Identify the blood parasite species.
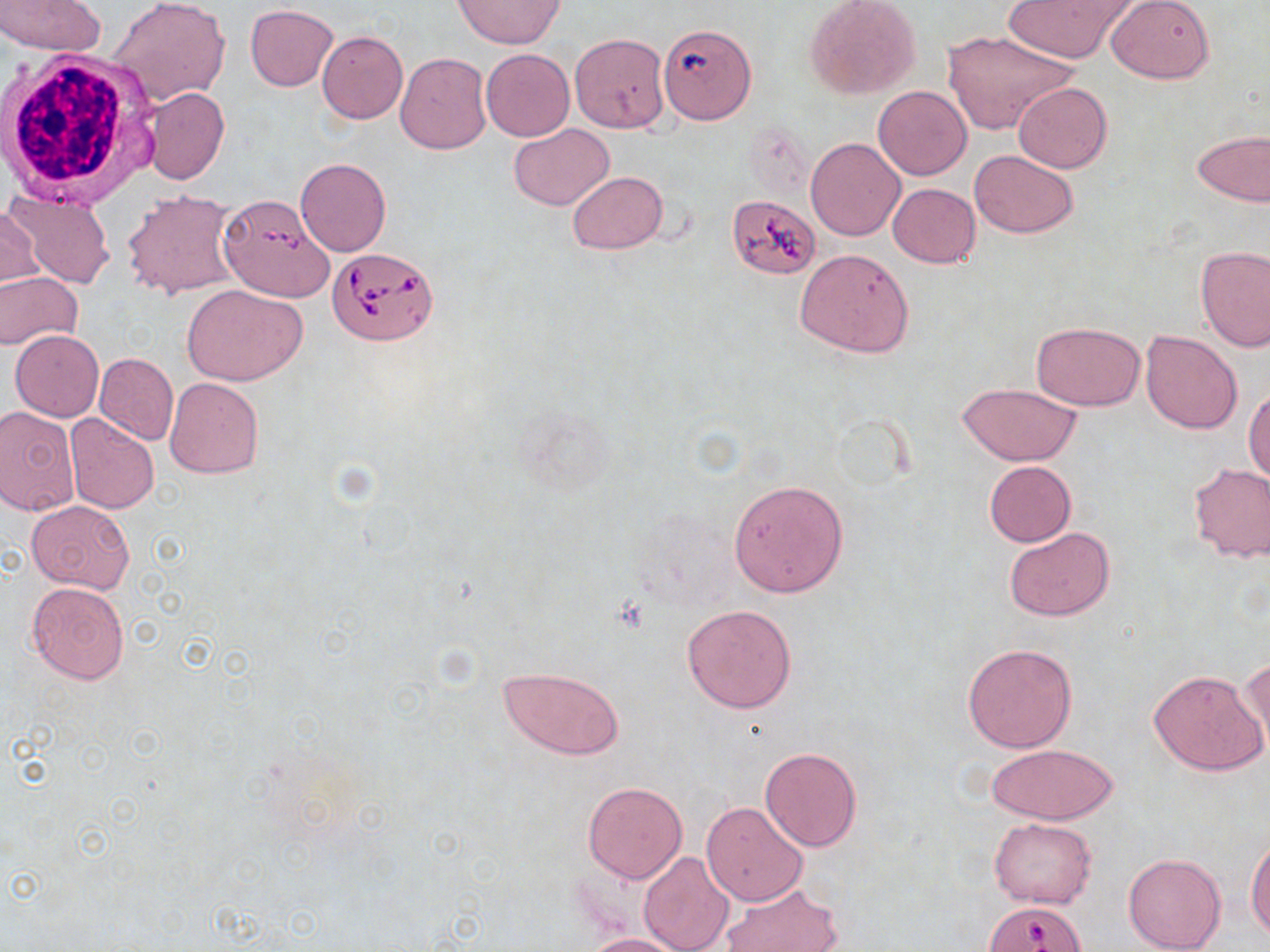

Babesia divergens.

uninfected red blood cell locations = approximate bounding boxes as (x1, y1, x2, y2) in pixels: (109, 0, 230, 108), (1004, 0, 1134, 63), (1106, 0, 1214, 85), (0, 1, 107, 55), (453, 1, 564, 49), (806, 2, 922, 99), (246, 4, 337, 91), (657, 21, 757, 125), (940, 29, 1079, 137), (317, 31, 408, 123), (570, 32, 670, 133), (481, 49, 574, 141), (395, 52, 491, 154), (1013, 82, 1112, 172), (873, 85, 972, 180), (142, 86, 230, 185), (508, 123, 614, 211), (1192, 128, 1270, 207), (806, 137, 905, 241), (971, 150, 1079, 239), (295, 157, 391, 257), (567, 171, 667, 254), (887, 184, 981, 268), (3, 187, 115, 289), (123, 189, 240, 298), (723, 194, 819, 277), (224, 198, 334, 298), (1, 207, 42, 290), (1195, 245, 1269, 351), (795, 249, 914, 358), (0, 272, 83, 351), (182, 284, 308, 386), (1031, 322, 1145, 411), (10, 331, 104, 420), (1140, 331, 1243, 433), (93, 352, 178, 444), (165, 376, 264, 478), (954, 382, 1085, 466), (1245, 387, 1270, 486), (0, 405, 82, 516), (65, 414, 159, 514), (983, 461, 1077, 547), (1186, 463, 1270, 562), (729, 480, 848, 597), (26, 499, 134, 595), (1004, 528, 1114, 622), (26, 582, 129, 683), (682, 604, 796, 714), (961, 642, 1077, 752), (1240, 658, 1270, 754), (499, 665, 623, 760), (1148, 670, 1267, 776), (986, 743, 1118, 824), (759, 746, 864, 851), (582, 781, 687, 883), (702, 802, 808, 905), (989, 817, 1097, 909), (1247, 836, 1269, 940), (638, 851, 734, 952), (1123, 852, 1226, 952), (720, 880, 843, 952), (582, 933, 694, 952)
white blood cell locations = approximate bounding boxes as (x1, y1, x2, y2) in pixels: (1, 48, 157, 207)
magnification = 1000x
field of view = one of a larger specimen
stain = May-Grünwald-Giemsa
preparation = thin blood smear
Babesia divergens-infected red blood cell locations = approximate bounding boxes as (x1, y1, x2, y2) in pixels: (327, 245, 438, 346)
image size = 1270×952 pixels
modality = light microscopy